Assess this cell for malaria.
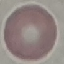
Uninfected.

Giemsa-stained preparation. Thin blood smear. Cell patch, automatically extracted from a larger field of view and resized to 64 × 64 pixels. Photographed with a smartphone camera at the microscope eyepiece.